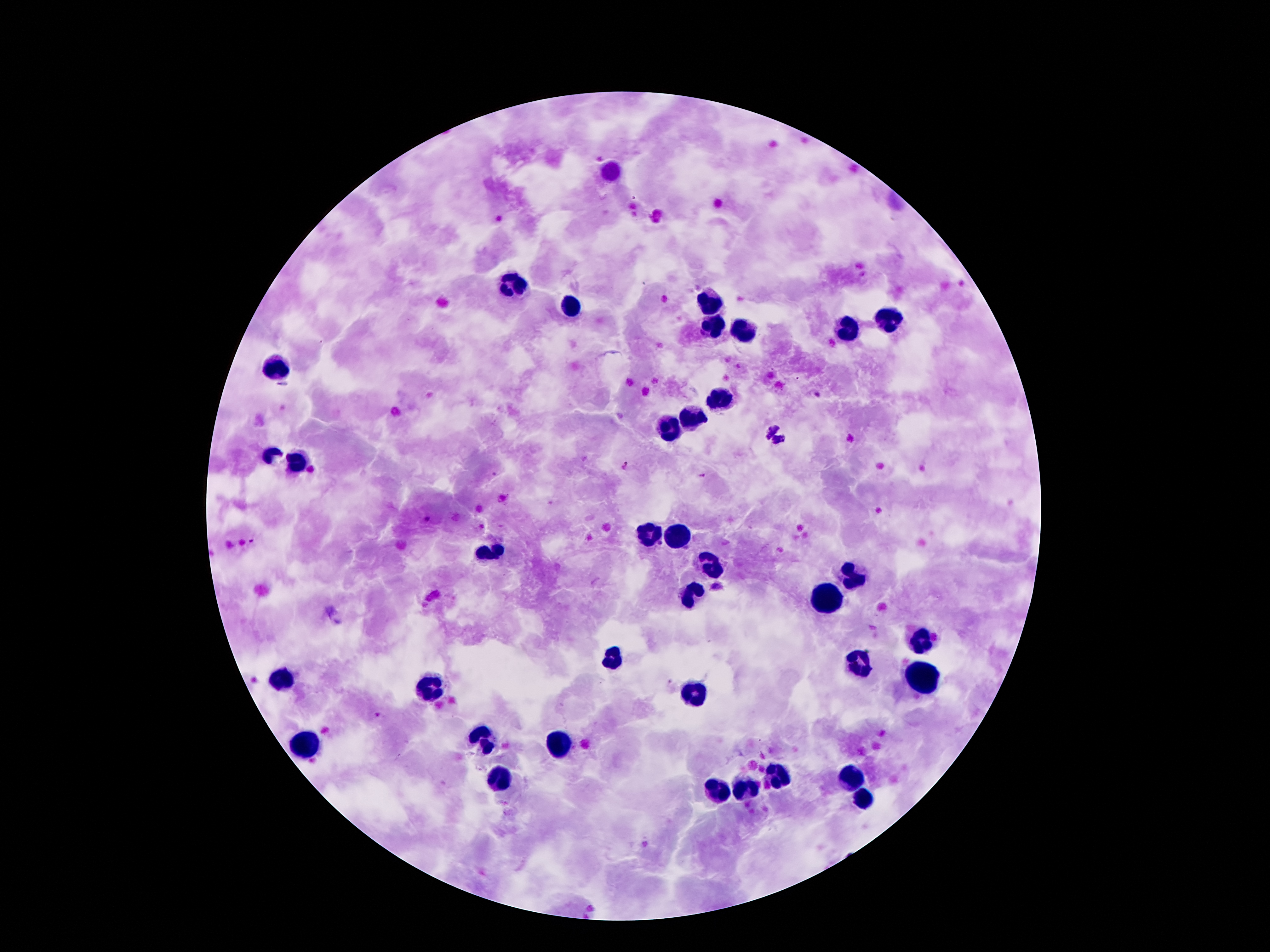

coordinate format = approximate centers as {x, y} in pixels
leukocyte locations = {610, 171}, {514, 287}, {708, 302}, {567, 305}, {886, 317}, {712, 329}, {741, 331}, {845, 331}, {272, 369}, {722, 398}, {694, 418}, {673, 432}, {272, 455}, {297, 463}, {647, 531}, {679, 538}, {489, 554}, {712, 560}, {853, 575}, {692, 593}, {827, 595}, {919, 639}, {613, 660}, {861, 663}, {922, 678}, {280, 681}, {428, 690}, {694, 696}, {482, 738}, {557, 746}, {306, 747}, {780, 778}, {848, 779}, {495, 783}, {746, 790}, {717, 791}, {865, 800}
malaria parasite locations = {765, 427}, {779, 440}, {625, 465}, {703, 476}, {426, 519}, {252, 540}, {660, 544}, {717, 587}
capture = smartphone camera through the microscope eyepiece
field of view = single
magnification = 100x
preparation = thick blood film
patient malaria status = infected with Plasmodium falciparum
stain = Giemsa
image size = 1270×952 pixels